State which parasite is depicted.
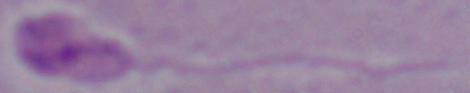
Leishmania.

Summary:
  - Modality: photomicrograph
  - Magnification: 1000x